Name the cell type shown.
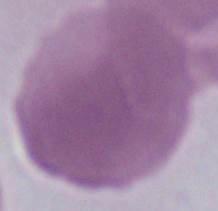

An erythrocyte.

Photomicrograph. Captured at 1000x magnification.